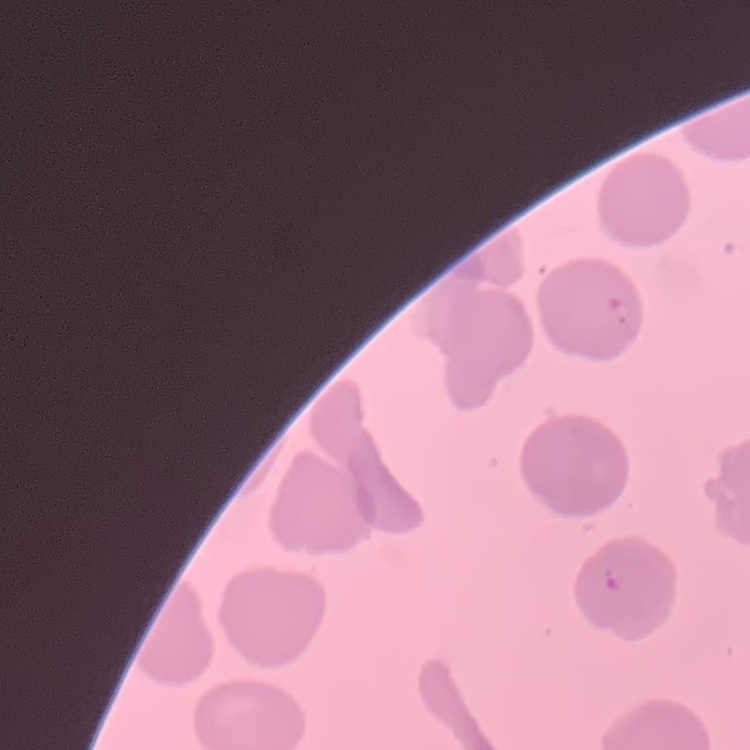
red blood cell morphology = no rouleaux formation
stain = Field's or Giemsa
preparation = thin peripheral smear
image type = square crop of a larger photomicrograph